Give the preparation type.
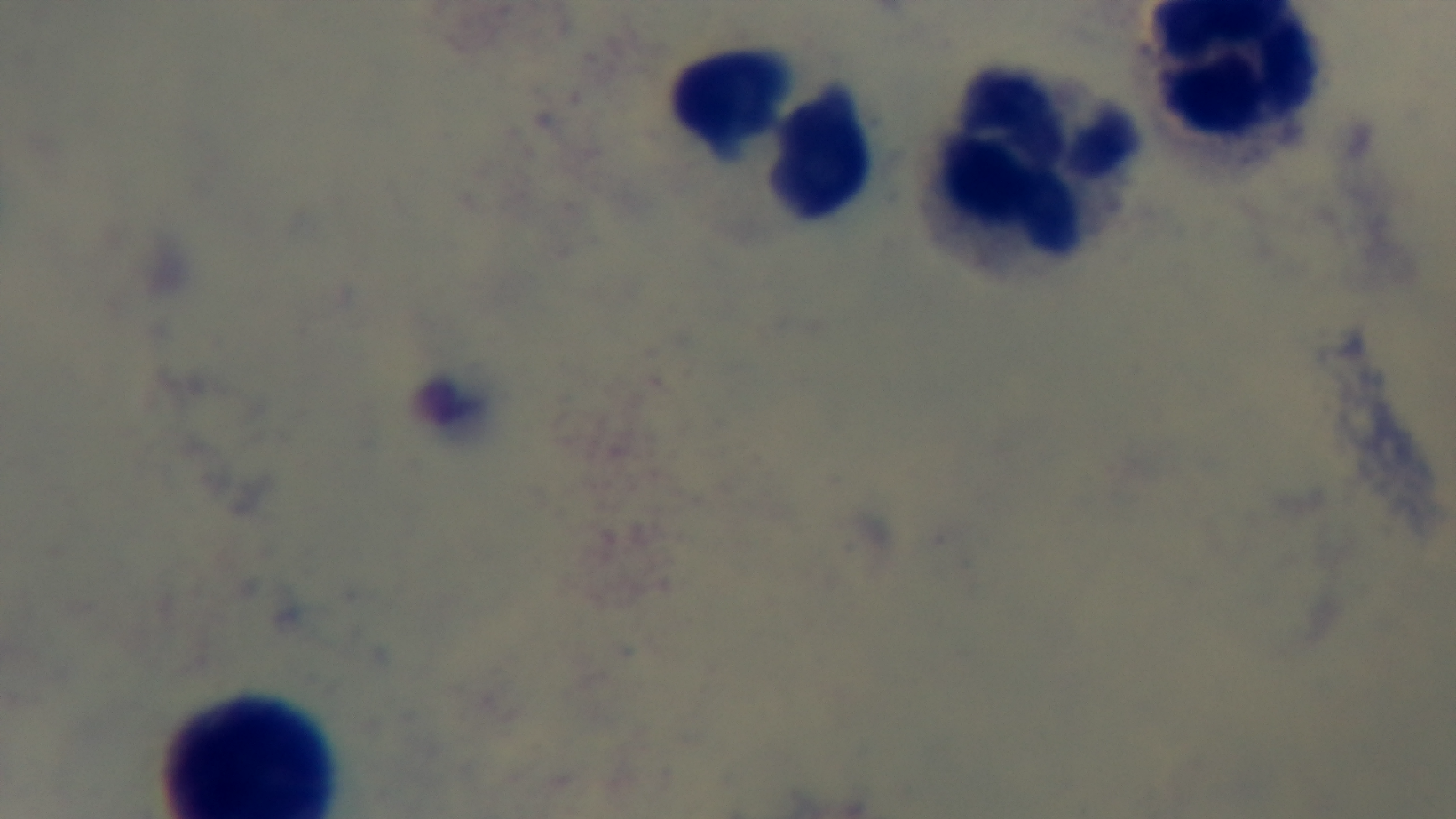

It is a thick blood film.

Summary:
  - Malaria status: uninfected
  - Field of view: single
  - Modality: light microscopy
  - Stain: Giemsa
  - Objective: 100x oil immersion
  - Capture: mounted 4K digital camera